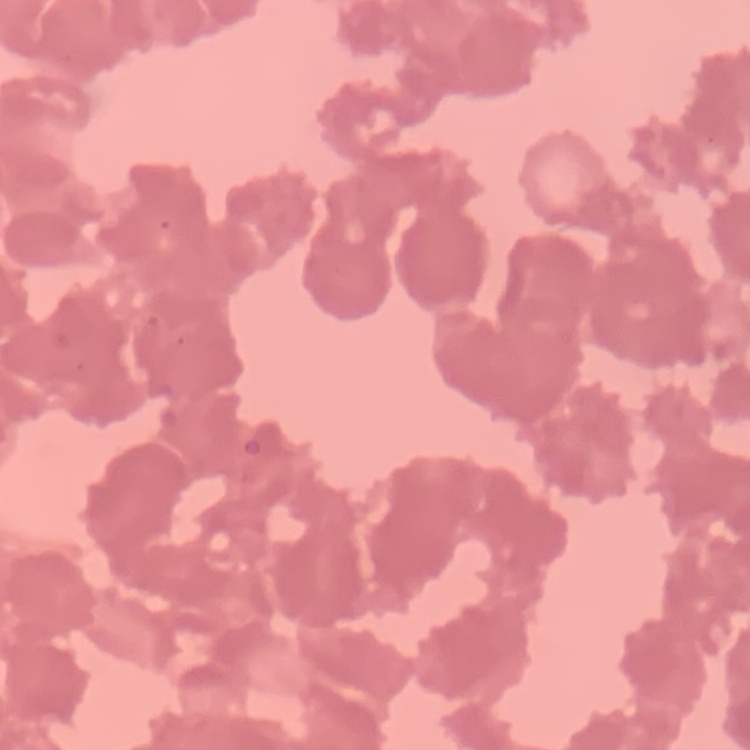
Summary:
  - Erythrocyte morphology: rouleaux formation
  - Image type: square crop of a larger photomicrograph
  - Stain: Field's or Giemsa
  - Preparation: thin peripheral smear